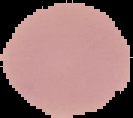
malaria status = uninfected
image size = 133×118 pixels
preparation = thin blood smear
image type = cell region segmented out of the field of view; surrounding area masked to black